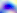

Summary:
  - Identification: Toxoplasma gondii
  - Magnification: 400x
  - Modality: photomicrograph